State which cell type is depicted.
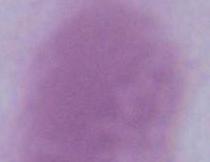

This is an erythrocyte.

magnification = 1000x
modality = photomicrograph